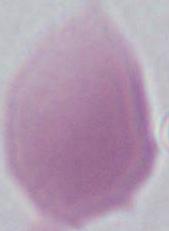

magnification = 1000x
identification = red blood cell
modality = photomicrograph